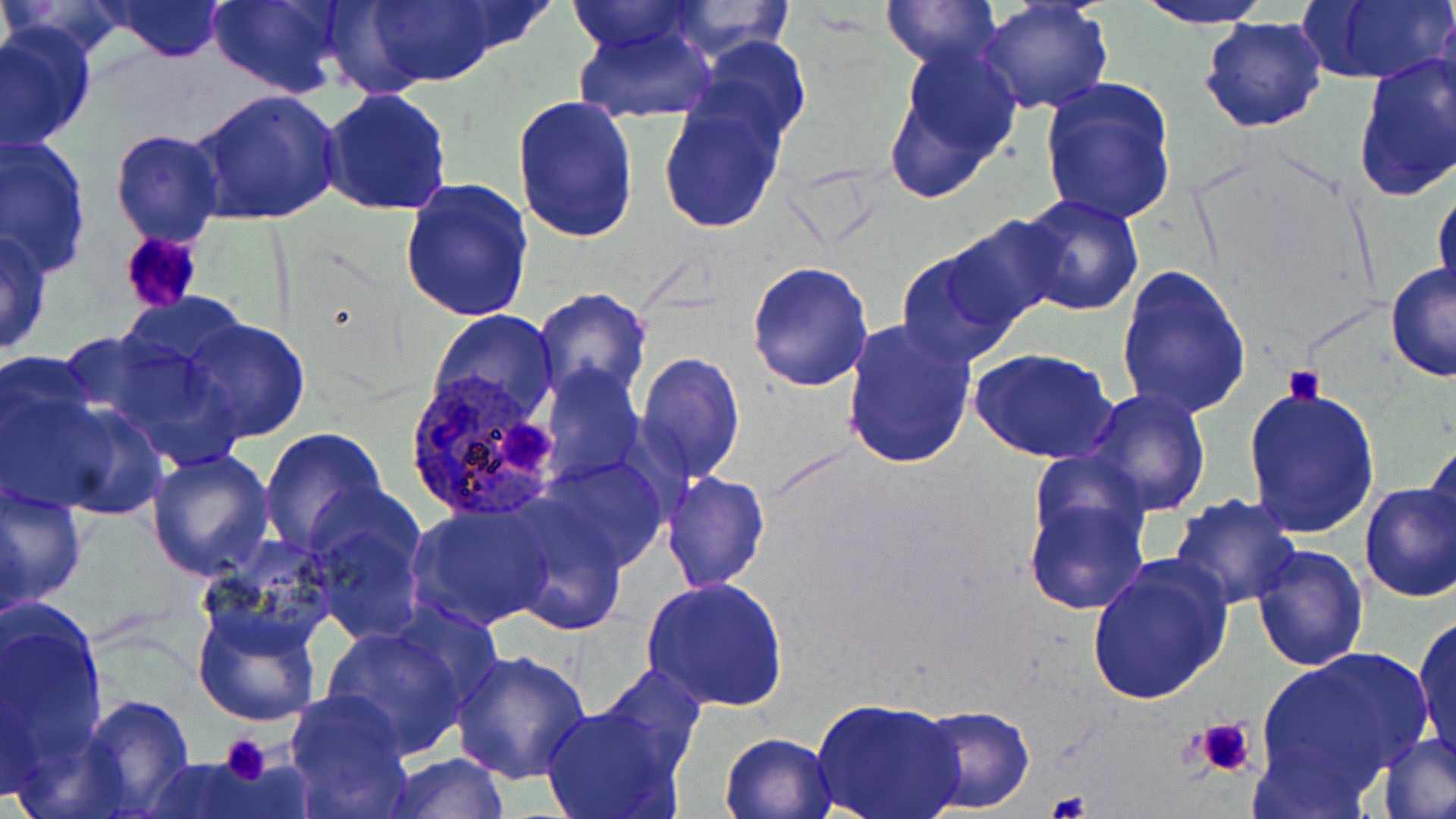 Approximate bounding boxes as [x1, y1, x2, y2] in pixels. Plasmodium ovale-infected red blood cell locations: [402, 370, 564, 521]. Uninfected red blood cell locations: [0, 0, 133, 64], [104, 0, 228, 62], [206, 0, 346, 100], [360, 0, 505, 88], [882, 0, 1000, 71], [1134, 0, 1277, 29], [1297, 0, 1455, 87], [563, 1, 707, 56], [660, 1, 797, 60], [977, 1, 1113, 115], [1434, 7, 1456, 122], [1200, 14, 1326, 133], [572, 23, 719, 124], [0, 24, 95, 154], [689, 34, 812, 151], [885, 43, 1022, 197], [1352, 53, 1456, 202], [1039, 75, 1178, 226], [320, 88, 452, 216], [191, 89, 343, 225], [658, 92, 788, 234], [512, 93, 640, 242], [109, 129, 224, 247], [1, 135, 94, 276], [399, 177, 534, 323], [1432, 184, 1456, 302], [1017, 193, 1144, 316], [940, 214, 1072, 332], [0, 228, 53, 357], [895, 248, 1026, 369], [747, 261, 875, 392], [1384, 264, 1456, 382], [1116, 265, 1251, 420], [532, 288, 653, 408], [116, 291, 253, 386], [431, 309, 558, 427], [839, 318, 978, 470], [181, 319, 310, 443], [76, 330, 252, 470], [971, 348, 1119, 462], [0, 349, 105, 510], [635, 350, 744, 483], [539, 364, 643, 485], [1242, 385, 1381, 539], [1081, 388, 1212, 517], [22, 389, 168, 523], [258, 428, 388, 556], [1423, 438, 1454, 552], [146, 448, 276, 581], [535, 456, 671, 574], [662, 472, 768, 593], [0, 481, 87, 612], [1021, 481, 1152, 616], [1359, 483, 1456, 602], [1169, 493, 1299, 609], [303, 497, 428, 644], [0, 498, 29, 630], [499, 500, 630, 637], [409, 504, 556, 630], [194, 533, 343, 659], [1251, 544, 1369, 672], [1084, 556, 1233, 707], [641, 576, 788, 712], [1, 604, 109, 781], [193, 605, 322, 727], [1411, 612, 1456, 763], [321, 622, 475, 758], [451, 647, 591, 784], [1257, 647, 1433, 792], [595, 664, 707, 776], [286, 691, 416, 818], [78, 694, 196, 819], [812, 696, 965, 819], [1330, 699, 1451, 814], [913, 703, 1035, 814], [540, 704, 686, 819], [719, 731, 838, 819], [1376, 734, 1456, 819], [384, 752, 510, 818], [138, 757, 273, 818]. Platelet locations: [118, 231, 203, 315], [1283, 364, 1325, 405], [503, 417, 557, 477], [1193, 716, 1259, 780], [217, 735, 271, 785], [1047, 791, 1092, 819]. Slide-level diagnosis: Plasmodium ovale. Thin blood film. May-Grünwald-Giemsa-stained preparation. Captured at 1000x magnification. Single field of view. Optical microscopy. Image is 1456×819 pixels.